Describe the morphology of the erythrocytes.
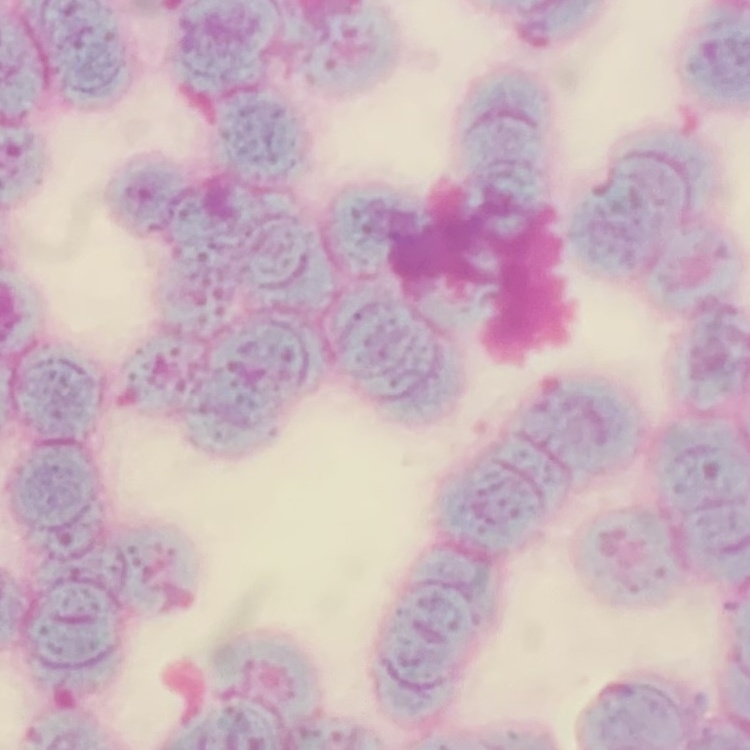

Rouleaux formation.

Summary:
  - Stain: Field's or Giemsa
  - Image type: square crop of a larger photomicrograph
  - Preparation: thin peripheral smear